Identify the parasite.
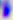
This is Toxoplasma gondii.

400x magnification. Micrograph.